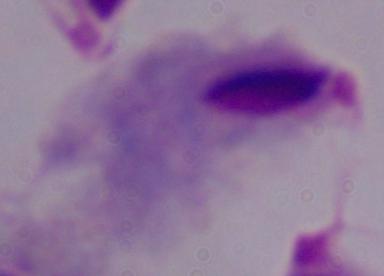

magnification = 1000x
identification = trichomonad
modality = micrograph